State which parasite is depicted.
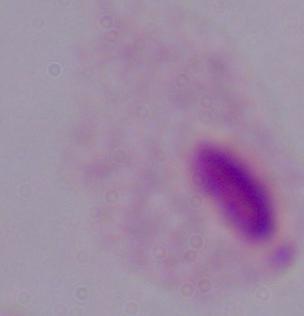
A trichomonad.

1000x magnification. Micrograph.